Assess this cell for malaria.
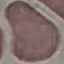
Uninfected.

Summary:
  - Image type: automatically extracted cell patch, resized to 64 × 64 pixels
  - Preparation: thin smear
  - Capture: smartphone camera at the microscope eyepiece
  - Stain: Giemsa